Identify the cell.
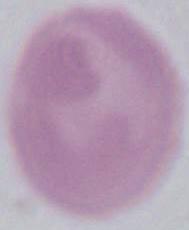

An erythrocyte.

Captured at 1000x magnification. Photomicrograph.